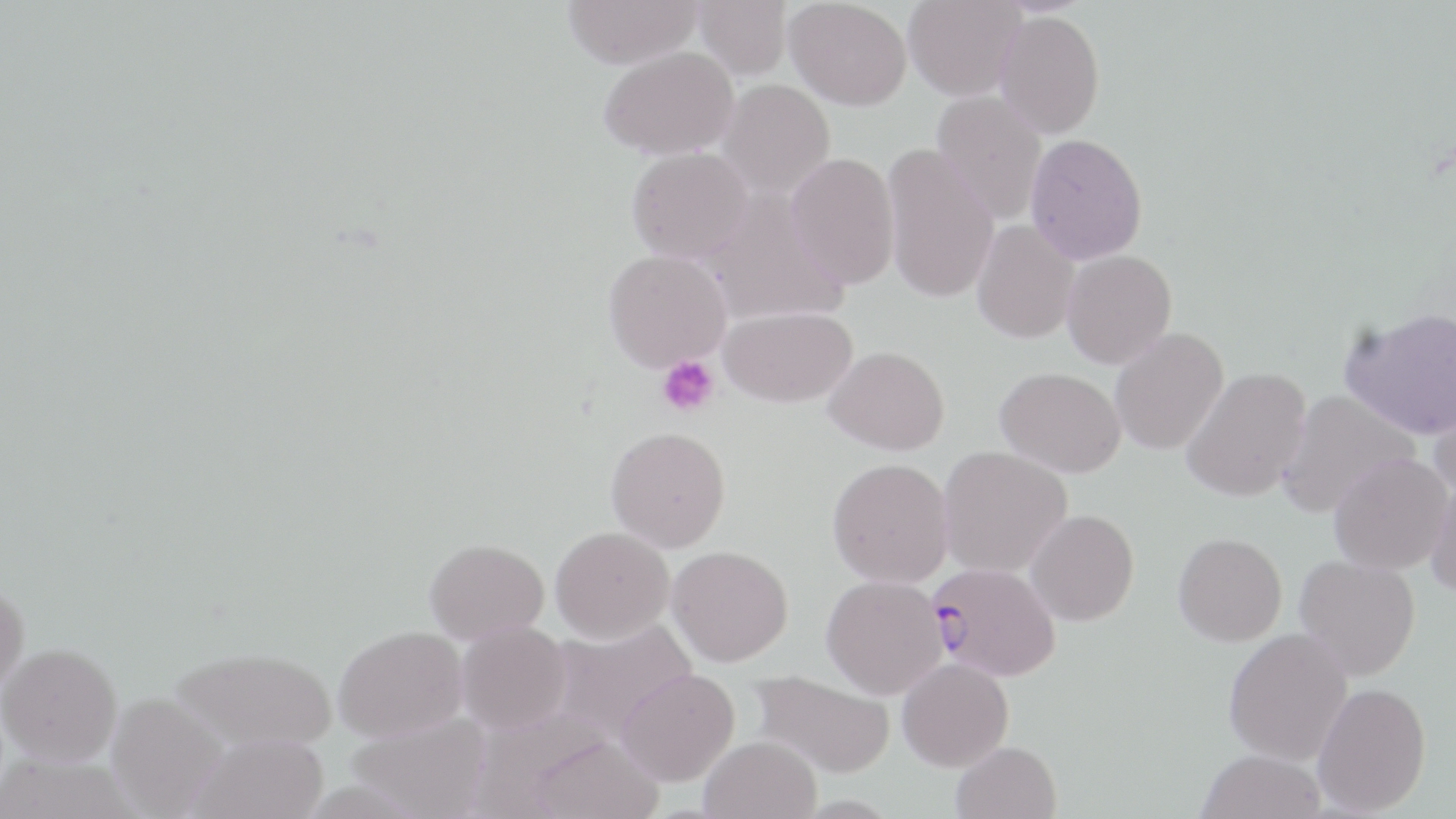

Summary:
  - Coordinate format: approximate bounding boxes as (x1, y1, x2, y2) in pixels
  - Platelet locations: (656, 355, 720, 417)
  - Plasmodium falciparum-infected red blood cell locations: (928, 562, 1061, 681)
  - Uninfected red blood cell locations: (562, 0, 703, 69), (693, 0, 792, 79), (785, 0, 912, 111), (903, 0, 1026, 101), (994, 9, 1104, 139), (598, 46, 738, 159), (718, 79, 835, 201), (931, 91, 1048, 224), (1025, 133, 1148, 264), (882, 144, 999, 303), (626, 147, 754, 264), (786, 152, 900, 290), (700, 190, 848, 326), (971, 219, 1080, 343), (603, 249, 731, 371), (1061, 249, 1177, 369), (720, 305, 858, 407), (1339, 305, 1456, 440), (1109, 327, 1229, 455), (824, 345, 950, 455), (995, 366, 1127, 478), (1181, 366, 1311, 502), (1428, 383, 1456, 500), (1276, 389, 1419, 518), (606, 426, 731, 551), (937, 445, 1072, 578), (1328, 453, 1453, 574), (827, 457, 953, 586), (1427, 473, 1456, 598), (1026, 509, 1139, 626), (551, 526, 674, 643), (1173, 532, 1287, 646), (424, 538, 549, 644), (667, 545, 793, 666), (1294, 555, 1420, 681), (821, 575, 947, 699), (0, 580, 28, 700), (548, 618, 699, 742), (456, 620, 571, 734), (333, 625, 467, 741), (1223, 627, 1353, 764), (1, 642, 122, 767), (170, 646, 337, 751), (897, 658, 1013, 771), (617, 668, 739, 786), (749, 669, 895, 778), (1313, 682, 1431, 815), (106, 692, 228, 818), (347, 712, 492, 819), (189, 733, 329, 819), (531, 734, 664, 819), (699, 735, 821, 819), (951, 741, 1062, 819), (1196, 748, 1326, 819)
  - Slide-level diagnosis: Plasmodium falciparum
  - Image size: 1456×819 pixels
  - Field of view: single
  - Modality: light microscopy
  - Preparation: thin blood film
  - Stain: May-Grünwald-Giemsa
  - Magnification: 1000x